Comment on the morphology of the red blood cells.
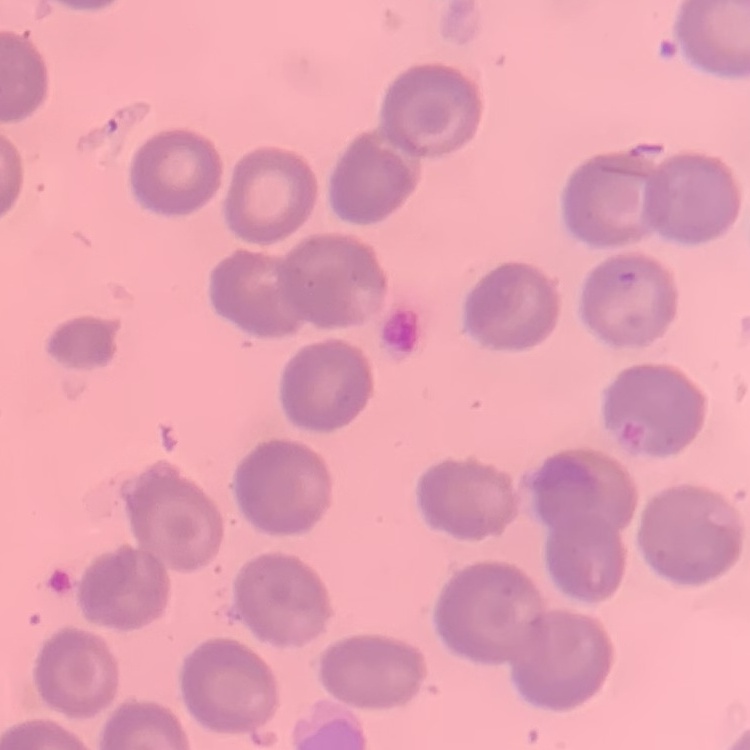

No rouleaux formation.

Summary:
  - Preparation: thin peripheral smear
  - Stain: Field's or Giemsa
  - Image type: square crop of a larger photomicrograph